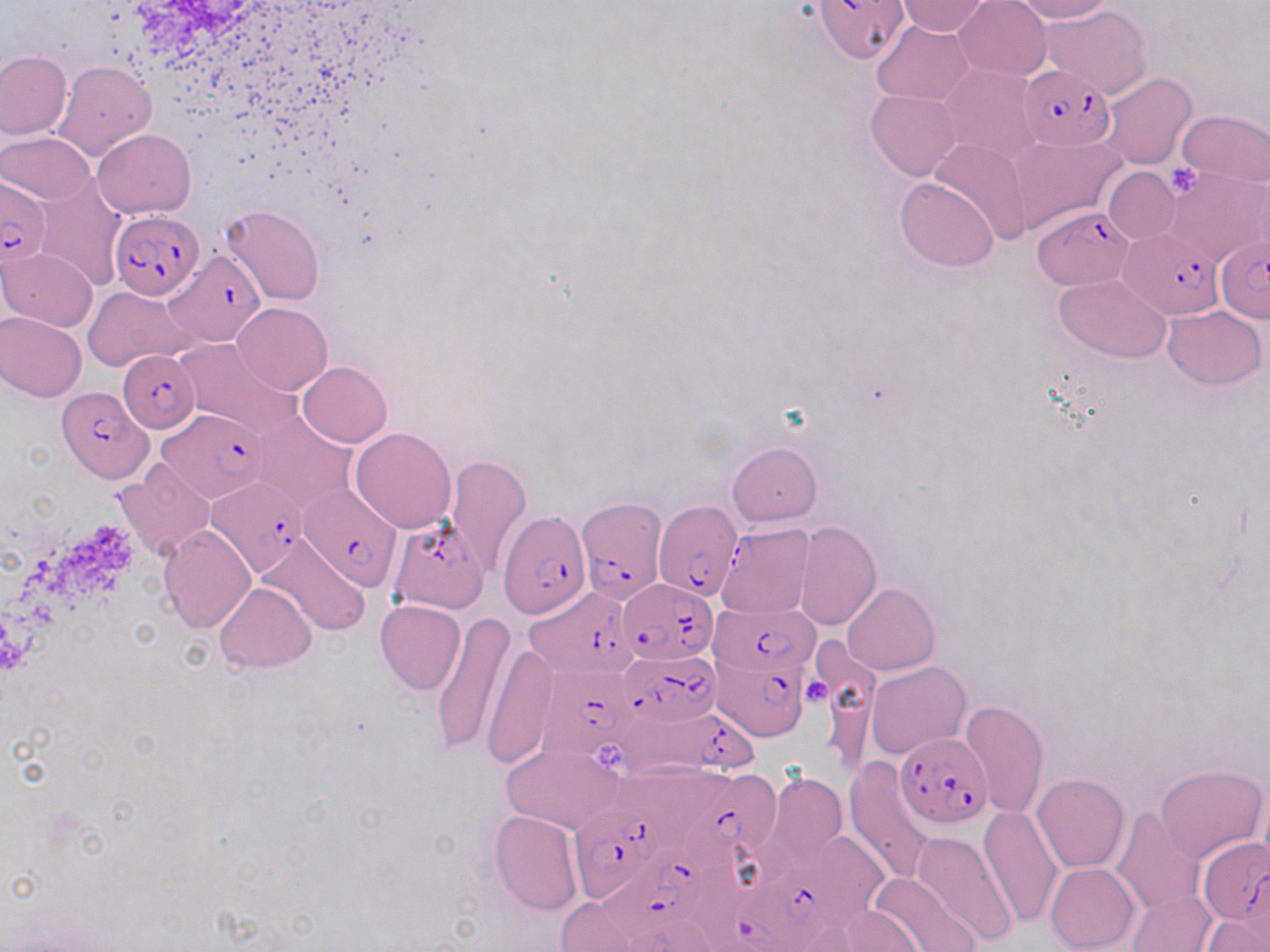

{
  "slide_level_diagnosis": "Plasmodium falciparum",
  "stain": "May-Grünwald-Giemsa",
  "image_size": "1270×952 pixels",
  "modality": "light microscopy",
  "uninfected_red_blood_cell_locations": "approximate bounding boxes as [x1, y1, x2, y2] in pixels: [894, 0, 993, 36], [953, 0, 1052, 81], [1008, 0, 1114, 24], [1041, 5, 1151, 98], [871, 20, 976, 105], [0, 51, 72, 140], [53, 60, 156, 162], [939, 64, 1042, 166], [1099, 72, 1198, 169], [866, 89, 962, 181], [1176, 110, 1269, 188], [92, 128, 195, 218], [2, 133, 95, 204], [1009, 136, 1124, 232], [929, 137, 1034, 244], [1102, 167, 1180, 243], [1164, 169, 1269, 269], [36, 177, 126, 291], [896, 177, 999, 272], [221, 205, 325, 306], [1, 247, 98, 331], [1055, 274, 1171, 362], [85, 286, 193, 373], [232, 302, 333, 394], [1162, 306, 1266, 388], [0, 311, 86, 402], [174, 339, 298, 436], [297, 361, 392, 447], [250, 412, 356, 512], [350, 426, 457, 533], [726, 441, 821, 527], [446, 455, 532, 576], [114, 461, 216, 560], [794, 522, 881, 630], [717, 523, 816, 620], [159, 524, 257, 633], [255, 534, 368, 638], [215, 581, 316, 672], [842, 583, 939, 675], [375, 600, 465, 695], [430, 611, 515, 757], [480, 639, 556, 768], [865, 661, 969, 761], [960, 699, 1049, 818], [500, 742, 626, 835], [845, 757, 938, 882], [1155, 763, 1267, 863], [769, 773, 845, 861], [1031, 773, 1130, 873], [1256, 779, 1270, 873], [978, 807, 1064, 928], [1111, 807, 1204, 915], [489, 810, 583, 915], [912, 831, 1018, 948], [1045, 862, 1139, 951], [866, 871, 977, 952], [1128, 888, 1216, 952], [550, 895, 658, 950], [820, 906, 927, 952], [1201, 914, 1266, 952]",
  "preparation": "thin blood smear",
  "field_of_view": "one of a larger specimen",
  "magnification": "1000x",
  "platelet_locations": "approximate bounding boxes as [x1, y1, x2, y2] in pixels: [1166, 164, 1201, 197], [804, 679, 833, 708], [594, 744, 627, 772]",
  "plasmodium_falciparum_infected_red_blood_cell_locations": "approximate bounding boxes as [x1, y1, x2, y2] in pixels: [813, 0, 908, 67], [1020, 65, 1117, 151], [0, 177, 52, 267], [1033, 206, 1136, 289], [110, 210, 204, 300], [1118, 231, 1226, 320], [1215, 235, 1270, 323], [164, 249, 267, 346], [117, 349, 200, 432], [59, 385, 153, 481], [156, 410, 267, 503], [205, 478, 309, 578], [300, 483, 401, 591], [578, 497, 670, 611], [652, 499, 744, 597], [498, 508, 592, 619], [388, 520, 488, 613], [620, 579, 717, 664], [522, 587, 640, 677], [709, 603, 820, 678], [618, 649, 721, 727], [710, 650, 810, 742], [543, 666, 642, 754], [615, 701, 760, 780], [895, 732, 993, 828], [667, 773, 788, 869], [566, 799, 678, 905], [738, 834, 890, 935], [1198, 838, 1270, 929], [597, 846, 708, 947], [692, 869, 818, 952]"
}